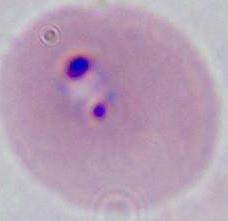
identification: Plasmodium
modality: micrograph
magnification: 400x or 1000x